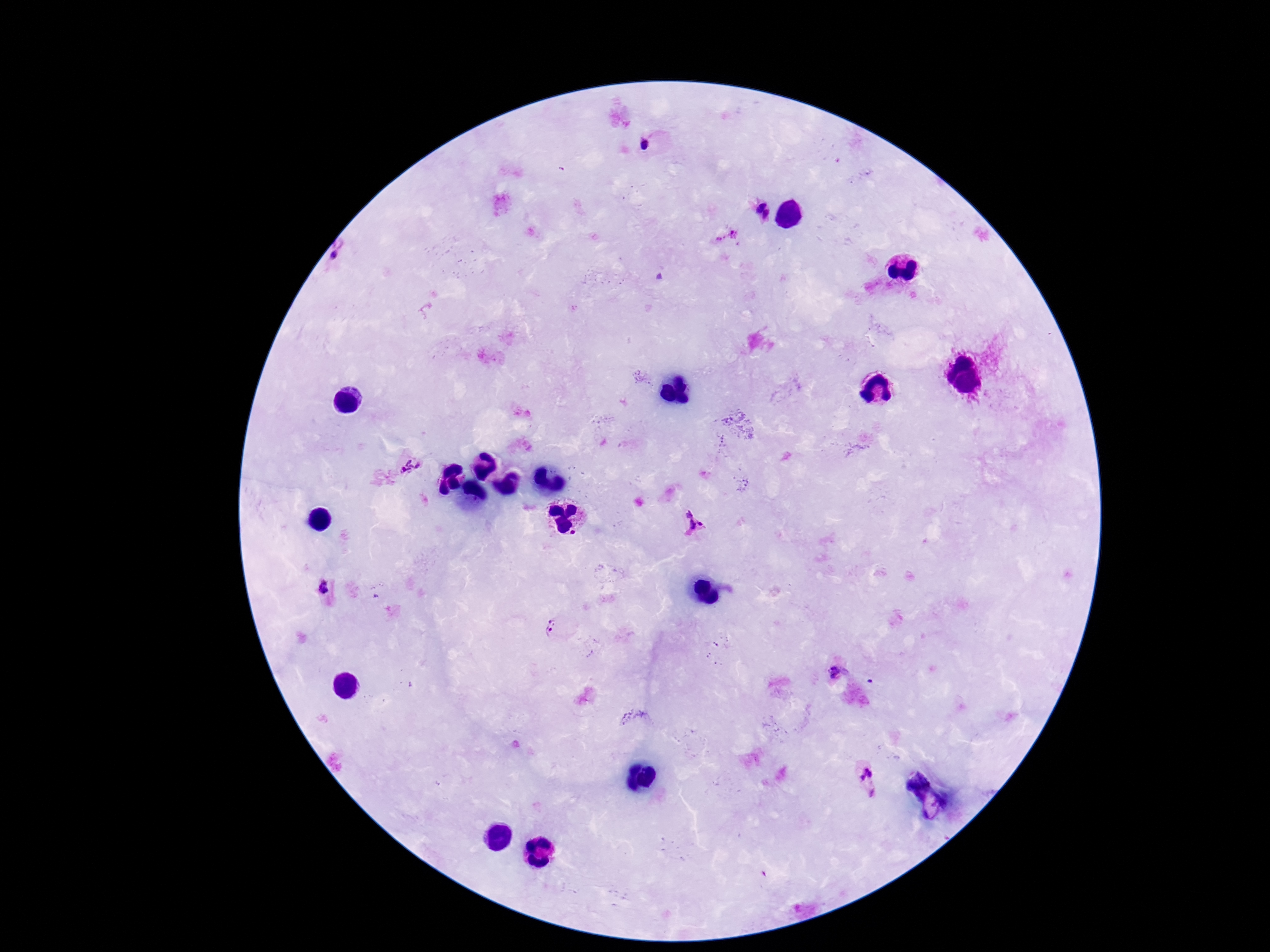

Approximate centers as {x, y} in pixels. Plasmodium parasite locations: {648, 144}, {757, 208}, {726, 235}, {342, 256}, {410, 467}, {693, 522}, {323, 586}, {552, 627}, {839, 672}, {870, 783}. Patient malaria status: positive. 100x magnification. Image is 1270×952 pixels. Photographed through the microscope eyepiece with a smartphone camera. Thick peripheral-blood smear. Giemsa stain. Single field of view.